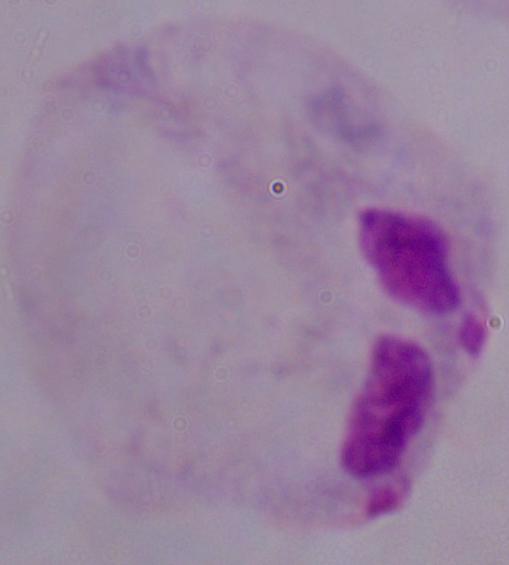

Summary:
  - Modality: photomicrograph
  - Identification: trichomonad
  - Magnification: 1000x